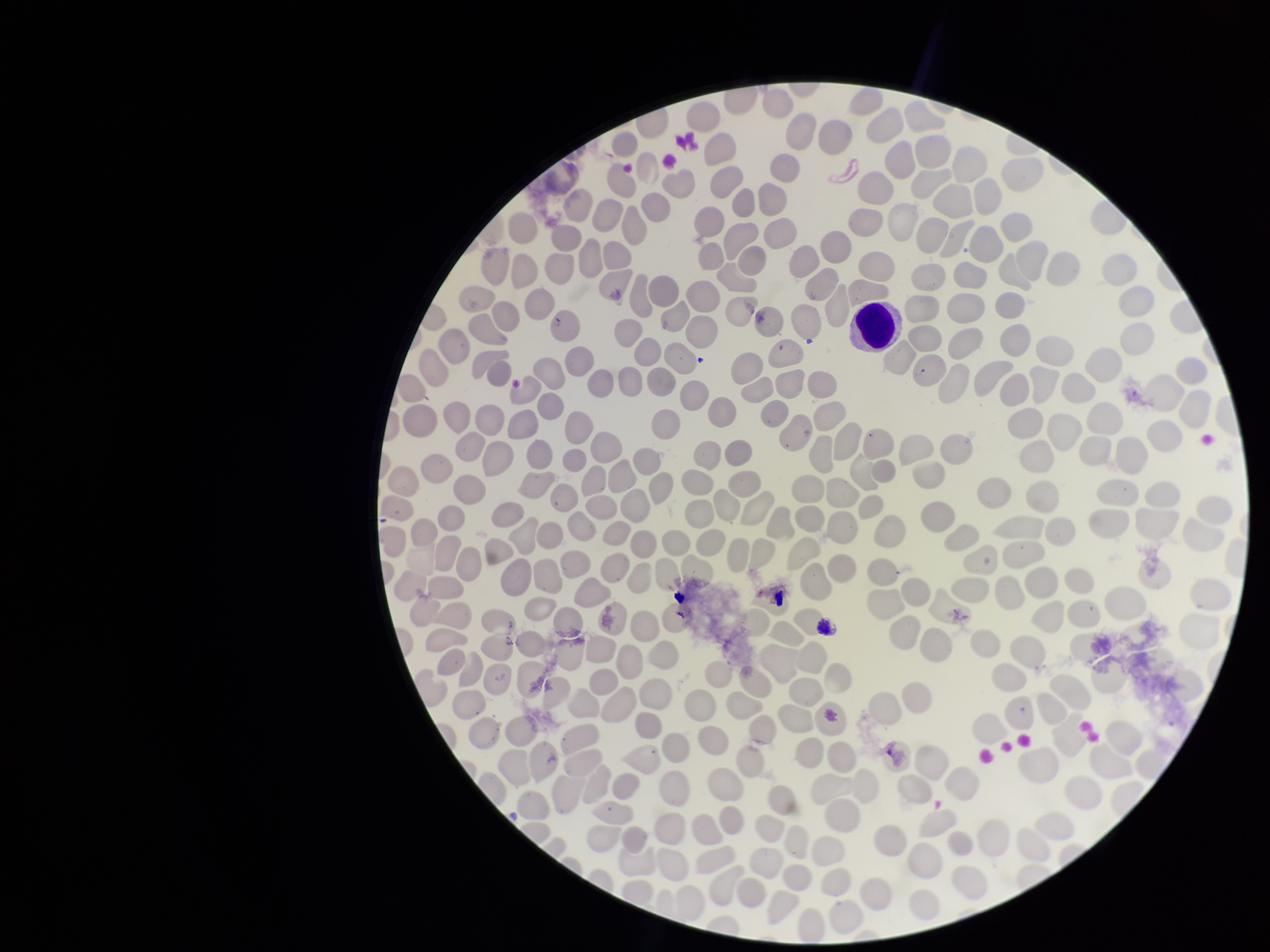 Preparation: thin smear. Stained with Giemsa. Parasitized red blood cell count: 0. Parasitized red blood cells: none detected. Image is 1270×952 pixels. Red blood cell count: 261. Patient malaria status: negative. Photographed through the microscope eyepiece with a smartphone camera. One field from this slide.